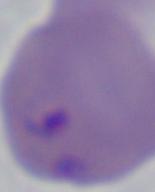
A Babesia parasite is shown. Micrograph. Captured at 1000x magnification.